Assess this cell for malaria.
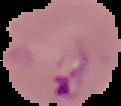

It is parasitized.

{
  "image_size": "121×106 pixels",
  "image_type": "segmented cell region on a black background",
  "preparation": "thin blood film"
}